Identify the cell.
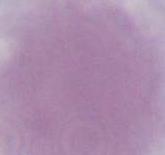

An erythrocyte.

Photomicrograph. Captured at 1000x magnification.